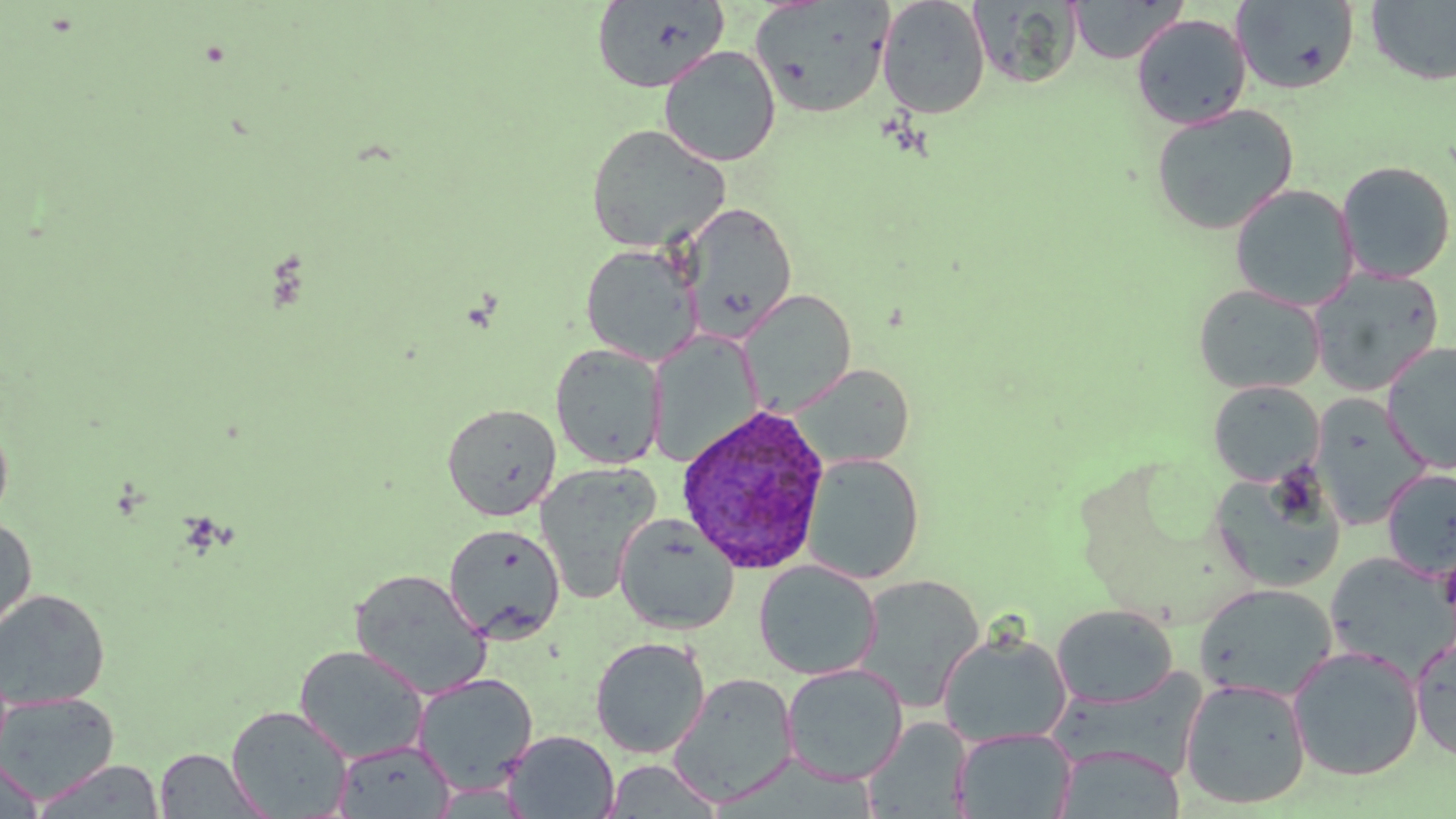
Summary:
  - Coordinate format: approximate bounding boxes as [x1, y1, x2, y2] in pixels
  - Uninfected red blood cell locations: [591, 0, 730, 93], [750, 0, 895, 119], [877, 0, 991, 119], [1068, 0, 1188, 64], [1231, 0, 1360, 95], [1365, 0, 1456, 86], [969, 1, 1082, 88], [1131, 13, 1252, 130], [658, 46, 781, 167], [1149, 103, 1300, 236], [585, 123, 731, 253], [1336, 160, 1455, 284], [1229, 183, 1358, 311], [681, 202, 796, 341], [580, 243, 704, 366], [1308, 268, 1445, 396], [1193, 283, 1325, 395], [737, 289, 857, 416], [646, 330, 762, 467], [1382, 340, 1455, 470], [550, 344, 667, 469], [790, 363, 915, 471], [1208, 381, 1324, 487], [1309, 394, 1431, 530], [442, 403, 561, 521], [0, 416, 14, 528], [802, 452, 925, 584], [534, 462, 661, 605], [1381, 468, 1455, 581], [1208, 469, 1347, 593], [614, 513, 739, 635], [0, 518, 37, 641], [443, 523, 566, 644], [1324, 551, 1456, 679], [753, 560, 881, 680], [349, 568, 493, 701], [853, 574, 985, 711], [1194, 583, 1338, 703], [0, 587, 111, 709], [1051, 604, 1179, 709], [937, 631, 1072, 748], [589, 636, 710, 758], [1410, 636, 1456, 763], [293, 644, 429, 764], [1287, 645, 1424, 782], [782, 663, 908, 785], [1052, 670, 1207, 779], [412, 672, 539, 795], [668, 673, 799, 808], [1179, 678, 1311, 810], [0, 691, 119, 804], [226, 705, 354, 818], [862, 718, 972, 817], [952, 727, 1076, 818], [502, 730, 620, 818], [332, 739, 456, 817], [1054, 745, 1186, 818], [154, 749, 269, 818], [0, 754, 45, 817], [32, 758, 164, 818], [604, 759, 722, 818]
  - Plasmodium ovale-infected red blood cell locations: [676, 403, 832, 575]
  - Slide-level diagnosis: Plasmodium ovale
  - Image size: 1456×819 pixels
  - Magnification: 1000x
  - Stain: May-Grünwald-Giemsa
  - Modality: optical microscopy
  - Preparation: thin blood film
  - Field of view: single